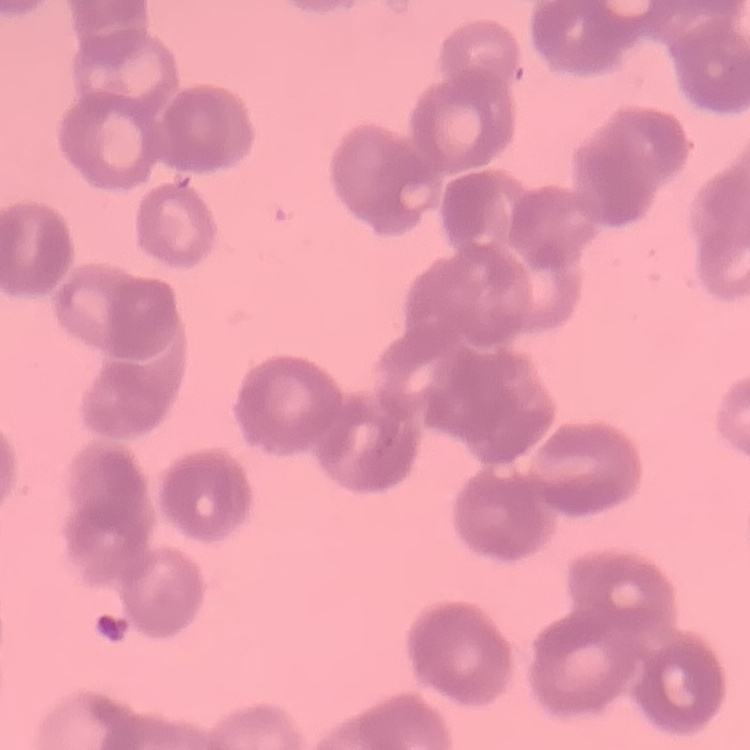

red_blood_cell_morphology: rouleaux formation
stain: Field's or Giemsa
preparation: thin peripheral smear
image_type: square crop of a larger photomicrograph